Report the malaria status of this cell.
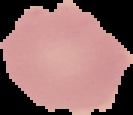

Uninfected.

The area outside the segmented cell region is set to black. From a thin blood film. Image is 133×115 pixels.